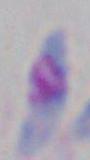

Micrograph. 1000x magnification. Toxoplasma gondii is shown.